Give the extent of all Plasmodium malariae-infected red blood cells.
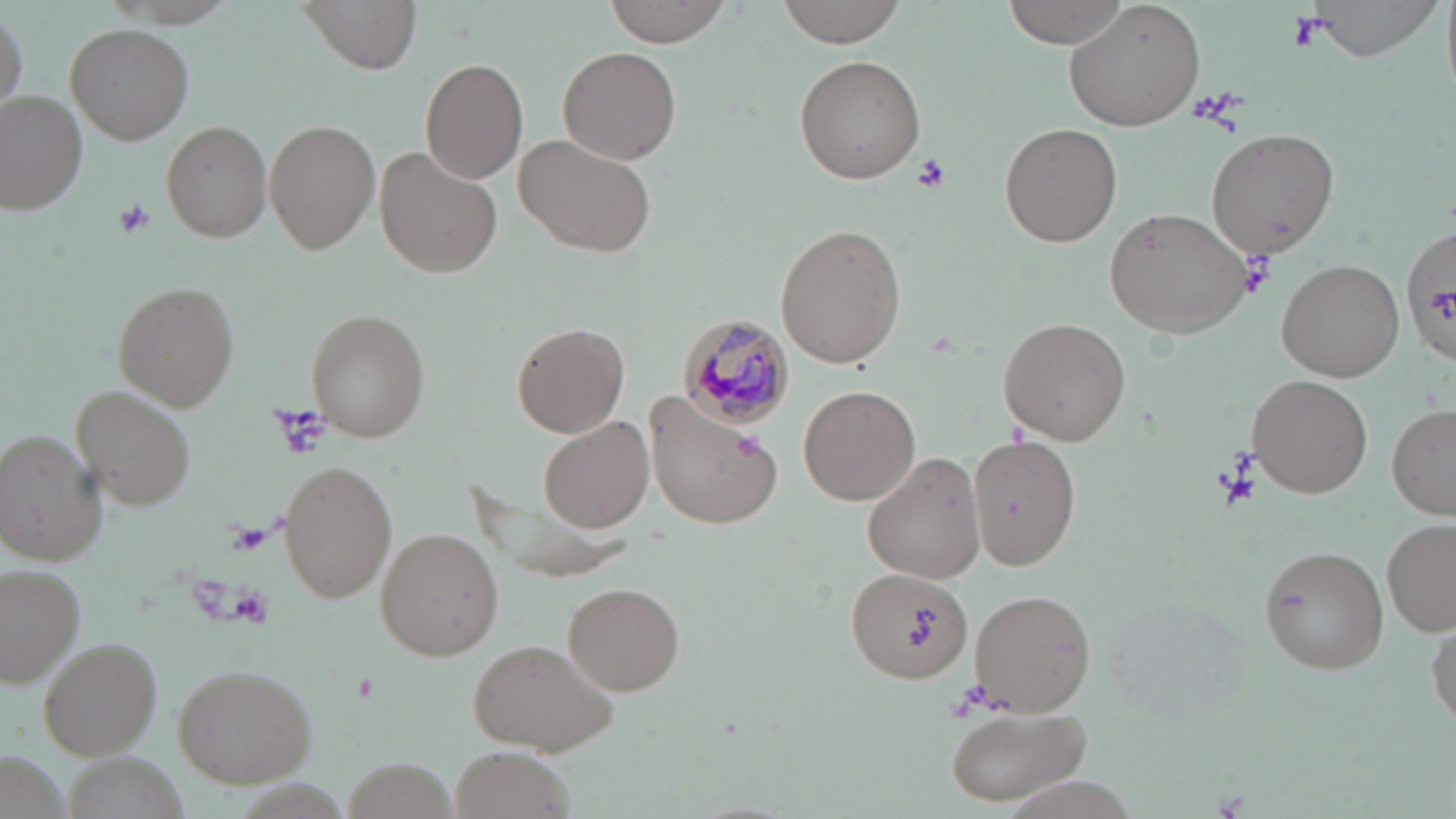
Approximate bounding boxes as (x1,y1)-(x2,y2) corner pairs in pixels.
Plasmodium malariae-infected red blood cells: (673,312)-(796,426).

slide-level diagnosis = Plasmodium malariae
magnification = 1000x
preparation = thin blood smear
platelet locations = approximate bounding boxes as (x1,y1)-(x2,y2) corner pairs in pixels: (1285,12)-(1327,53), (911,153)-(951,193), (110,198)-(154,239), (1238,252)-(1276,298), (1213,468)-(1262,514), (228,524)-(272,554)
uninfected red blood cell locations = approximate bounding boxes as (x1,y1)-(x2,y2) corner pairs in pixels: (300,0)-(420,74), (604,0)-(733,46), (776,0)-(914,46), (1004,0)-(1133,49), (1307,0)-(1442,62), (1063,2)-(1207,130), (1,4)-(26,121), (67,24)-(193,143), (559,46)-(681,165), (794,54)-(926,183), (418,58)-(530,183), (1,92)-(87,215), (263,119)-(380,254), (162,120)-(272,243), (1000,122)-(1122,247), (1207,129)-(1339,256), (517,134)-(658,258), (376,148)-(504,278), (1104,206)-(1253,338), (775,224)-(907,368), (1405,224)-(1456,365), (1276,258)-(1402,382), (113,282)-(239,410), (306,308)-(430,441), (998,318)-(1130,444), (512,321)-(632,437), (1248,374)-(1374,498), (798,385)-(920,506), (72,386)-(195,511), (643,390)-(784,532), (1386,403)-(1456,520), (537,413)-(654,534), (2,429)-(110,566), (967,435)-(1081,572), (863,452)-(986,585), (276,460)-(398,602), (1381,519)-(1455,636), (376,528)-(504,660), (1257,543)-(1388,676), (0,562)-(86,691), (845,568)-(975,688), (561,582)-(685,695), (968,588)-(1097,717), (1427,611)-(1456,734), (38,636)-(163,761), (465,638)-(619,756), (172,661)-(319,789), (945,703)-(1098,808), (448,747)-(580,819)
modality = optical microscopy
field of view = one of a larger specimen
stain = May-Grünwald-Giemsa
image size = 1456×819 pixels